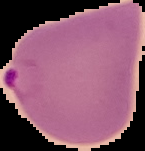

Summary:
  - Image size: 145×151 pixels
  - Preparation: thin blood film
  - Result: malaria parasites identified
  - Image type: segmented cell region with the area outside set to black